Assess this cell for malaria.
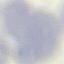
It is uninfected.

Giemsa-stained preparation. Automatically extracted cell patch, resized to 64 × 64 pixels. Thin blood film. Acquired by smartphone through the microscope eyepiece.